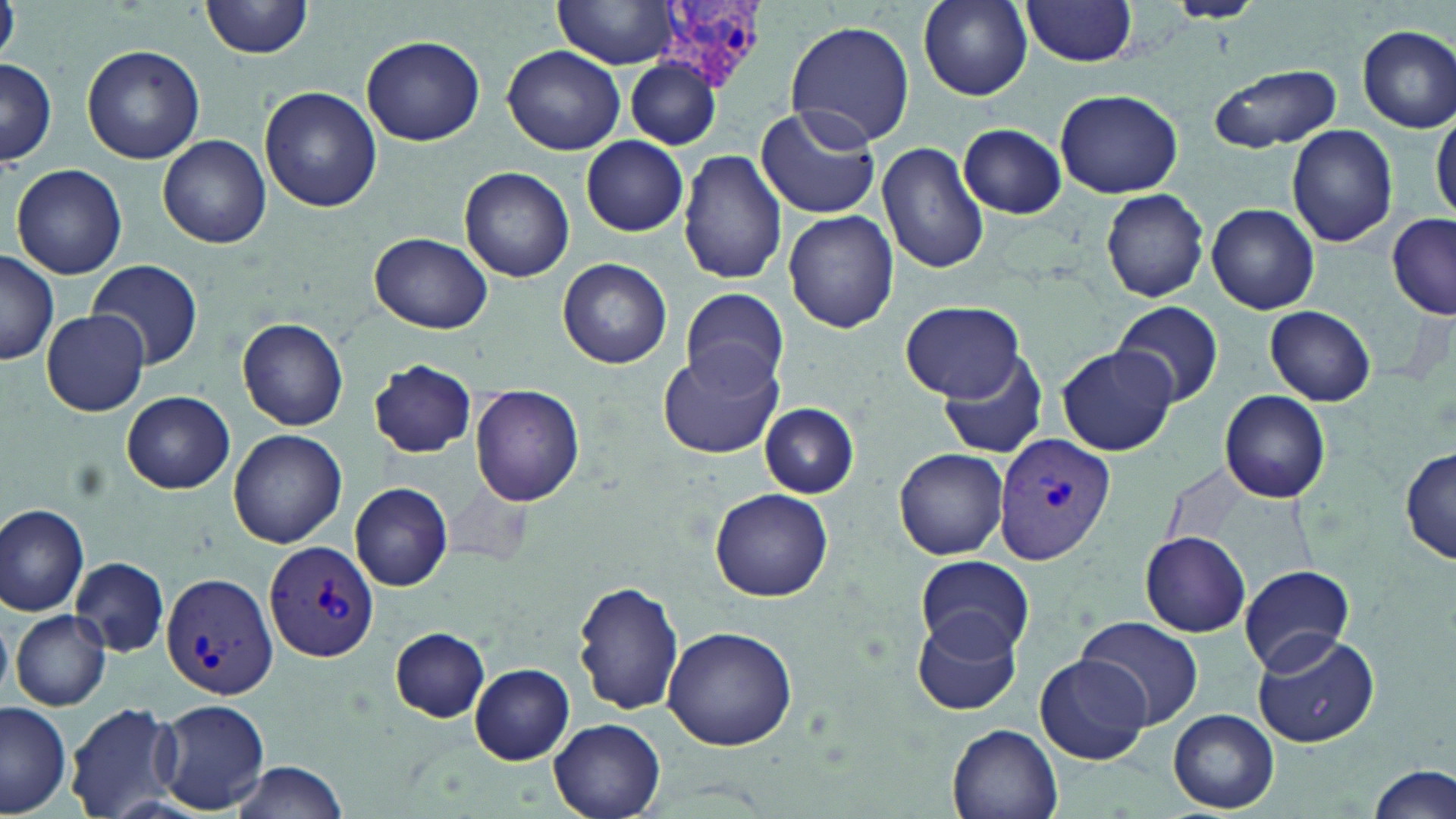

Approximate bounding boxes as (x1,y1)-(x2,y2) corner pairs in pixels. Plasmodium vivax-infected red blood cell locations: (662,0)-(766,93), (993,434)-(1115,564), (265,540)-(380,663), (160,570)-(279,700). Uninfected red blood cell locations: (200,0)-(317,60), (554,0)-(680,69), (918,0)-(1032,101), (1021,0)-(1140,67), (1163,0)-(1265,22), (783,18)-(915,147), (1357,26)-(1456,132), (362,35)-(485,146), (82,45)-(205,165), (503,45)-(625,155), (625,57)-(721,150), (1,59)-(58,166), (1208,62)-(1341,152), (260,86)-(381,212), (1055,88)-(1183,198), (756,103)-(880,220), (1431,109)-(1456,221), (959,123)-(1067,217), (1285,124)-(1398,247), (158,135)-(271,248), (581,137)-(688,236), (878,140)-(991,274), (679,150)-(789,285), (9,163)-(128,281), (460,167)-(574,281), (1099,188)-(1209,303), (1207,204)-(1319,314), (784,211)-(898,333), (1384,215)-(1456,320), (370,232)-(493,334), (0,252)-(59,365), (558,256)-(673,368), (85,257)-(205,370), (679,288)-(790,390), (1111,299)-(1224,407), (900,300)-(1023,400), (1265,305)-(1376,406), (41,311)-(150,415), (236,319)-(351,429), (658,346)-(783,459), (936,346)-(1049,460), (1056,346)-(1176,455), (370,360)-(477,458), (471,386)-(585,506), (1219,390)-(1332,501), (121,391)-(235,494), (759,403)-(859,497), (227,429)-(347,549), (895,448)-(1010,561), (1398,449)-(1455,564), (351,483)-(453,590), (710,488)-(833,603), (0,504)-(89,617), (1140,531)-(1251,637), (916,554)-(1034,659), (70,556)-(171,658), (1239,564)-(1355,673), (571,582)-(685,719), (9,610)-(112,712), (912,611)-(1023,717), (1072,614)-(1203,731), (663,626)-(798,752), (390,627)-(492,721), (1251,632)-(1381,748), (1035,653)-(1150,765), (470,663)-(574,764), (154,697)-(269,814), (65,701)-(183,818), (0,702)-(72,816), (1169,709)-(1279,813), (549,717)-(666,819), (947,723)-(1064,819), (224,760)-(349,818), (1369,763)-(1454,817). Slide-level diagnosis: Plasmodium vivax. May-Grünwald-Giemsa-stained preparation. Optical microscopy. One field of a larger specimen. Thin blood film. Captured at 1000x magnification. Image is 1456×819 pixels.